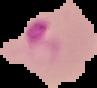
Malaria status: parasitized. From a thin blood smear. The area outside the segmented cell region is set to black. Image is 97×88 pixels.